Locate every uninfected red blood cell.
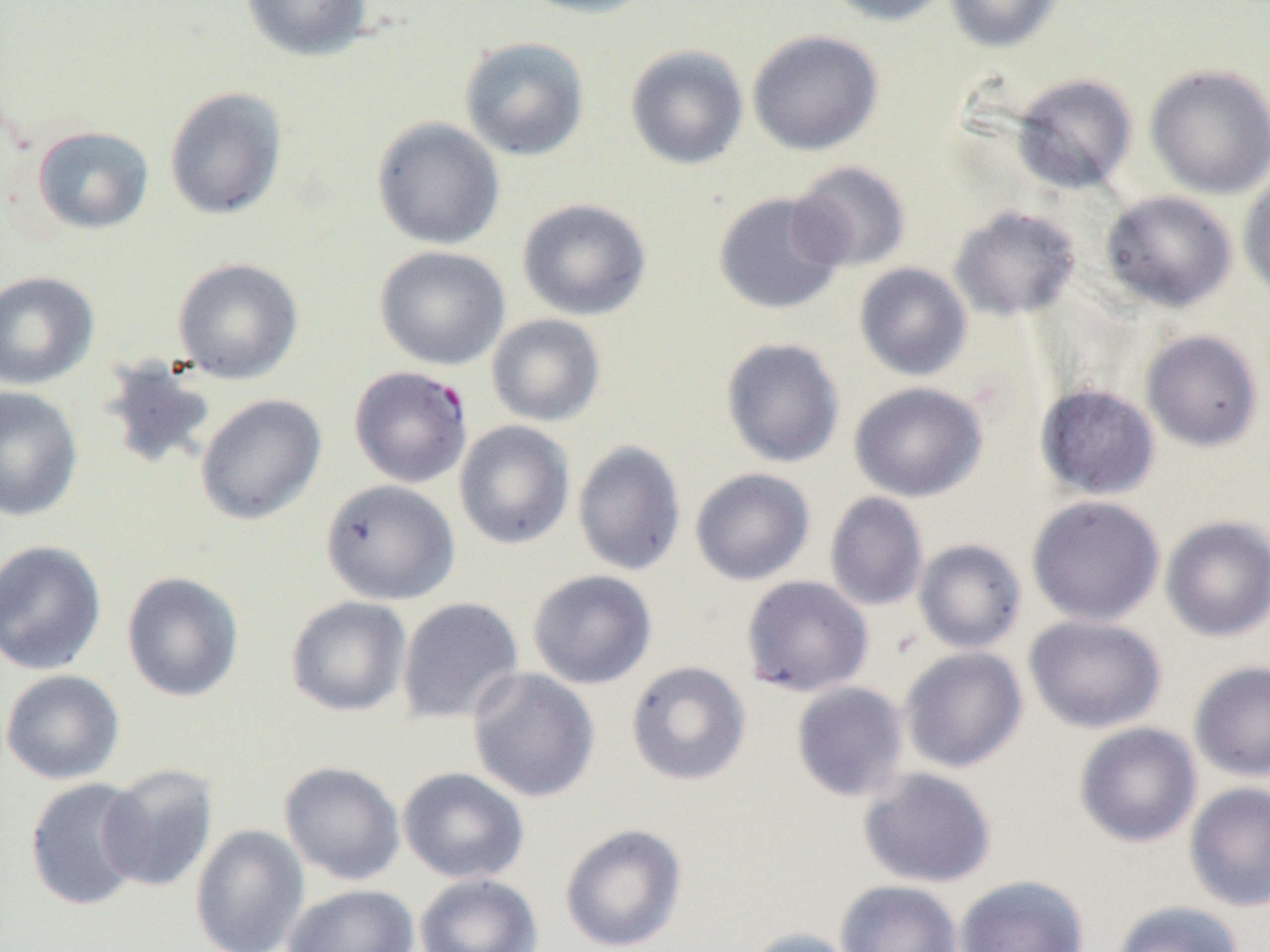

Approximate bounding boxes as (x1,y1)-(x2,y2) corner pairs in pixels.
Uninfected red blood cells: (242,0)-(371,61), (514,0)-(657,19), (820,0)-(953,26), (944,0)-(1064,53), (747,29)-(884,156), (459,36)-(590,162), (625,44)-(749,170), (1145,64)-(1270,199), (1011,74)-(1138,193), (164,87)-(288,220), (371,116)-(505,250), (31,125)-(154,235), (789,160)-(911,273), (1238,170)-(1270,304), (1101,190)-(1237,313), (712,191)-(847,315), (517,198)-(651,320), (949,206)-(1080,321), (374,245)-(510,370), (172,257)-(304,384), (854,262)-(972,381), (0,270)-(99,390), (486,313)-(606,427), (1141,330)-(1263,452), (721,337)-(845,468), (98,357)-(218,474), (849,381)-(987,501), (1035,383)-(1160,501), (0,386)-(82,521), (195,393)-(326,526), (454,420)-(575,550), (572,440)-(686,577), (690,467)-(815,585), (320,479)-(460,605), (825,492)-(928,612), (1027,495)-(1165,626), (1160,515)-(1270,642), (0,539)-(107,676), (913,539)-(1027,654), (527,569)-(657,689), (121,571)-(244,702), (741,575)-(873,697), (285,595)-(412,717), (397,597)-(524,724), (1024,614)-(1166,734), (899,646)-(1028,773), (1188,660)-(1270,781), (626,661)-(751,786), (467,668)-(600,802), (0,669)-(125,785), (791,682)-(909,802), (1075,722)-(1202,848), (279,761)-(406,885), (98,764)-(218,891), (397,767)-(529,885), (858,768)-(997,888), (24,777)-(147,911), (1184,781)-(1270,911), (559,823)-(688,952), (189,824)-(309,952), (415,873)-(543,952), (954,875)-(1090,952), (835,880)-(963,952), (282,884)-(420,952), (1111,900)-(1245,952), (741,927)-(861,952).

slide-level diagnosis = Plasmodium falciparum
preparation = thin blood film
modality = light microscopy
field of view = single
image size = 1270×952 pixels
magnification = 1000x
Plasmodium falciparum-infected red blood cell locations = approximate bounding boxes as (x1,y1)-(x2,y2) corner pairs in pixels: (348,365)-(473,488)